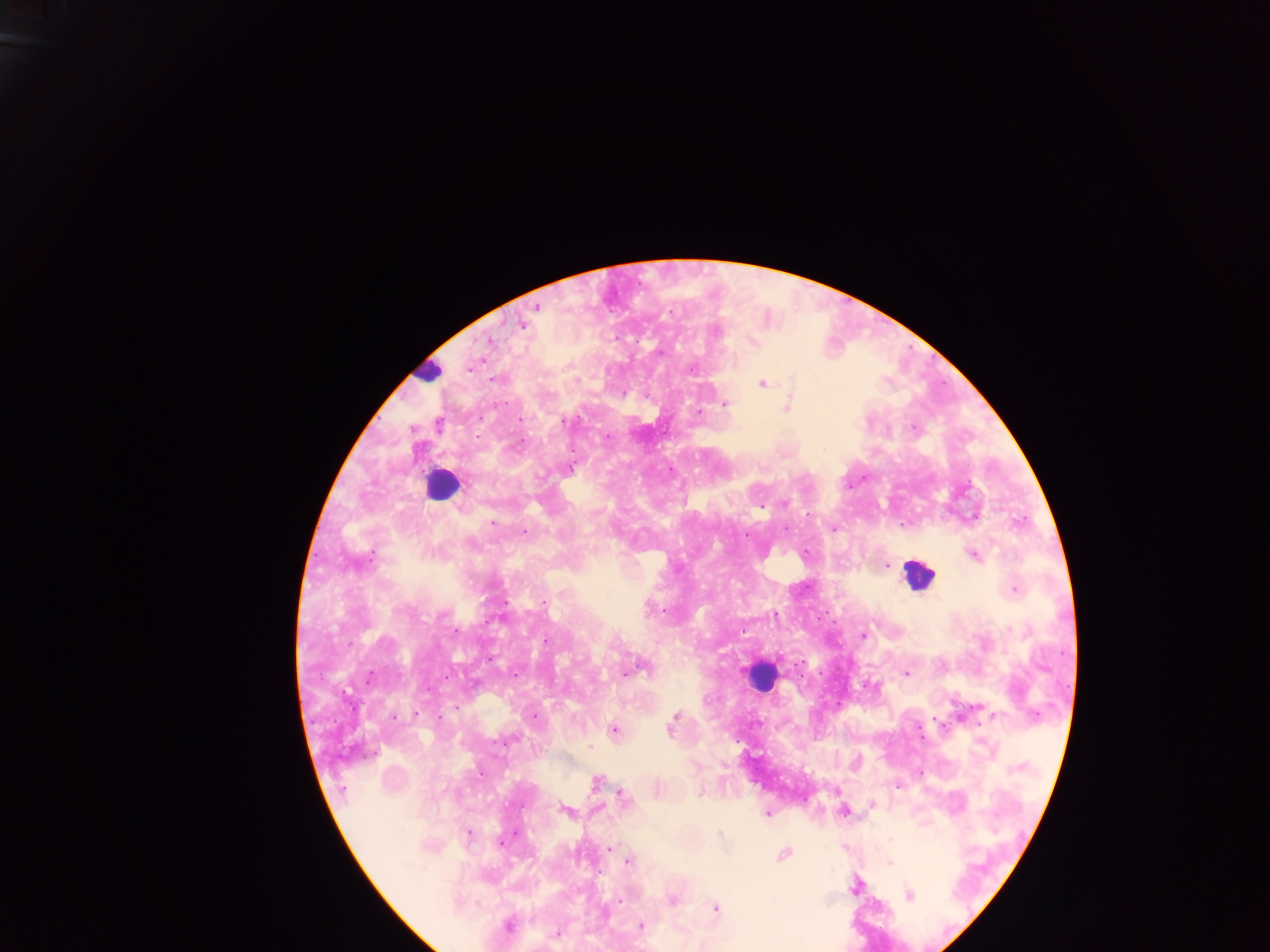 Approximate centers as (x, y) in pixels. Leukocyte locations: (427, 371), (442, 484), (918, 574), (761, 676). Malaria parasite locations: (536, 306), (521, 323), (717, 332), (490, 341), (754, 343), (493, 380), (763, 384), (724, 404), (786, 407), (519, 419), (563, 422), (439, 425), (607, 436), (571, 467), (784, 503), (493, 522), (833, 528), (524, 532), (973, 555), (372, 556), (887, 566), (1015, 589), (398, 611), (862, 635), (545, 642), (643, 668), (631, 671), (906, 674), (370, 675), (515, 675), (416, 714), (535, 716), (676, 716), (395, 717), (992, 717), (441, 718), (673, 722), (614, 730), (511, 740), (596, 782), (700, 793), (622, 798), (872, 804), (565, 810), (843, 811), (767, 813), (720, 834), (468, 835), (502, 841), (611, 849), (783, 855), (628, 861), (889, 863), (854, 887), (908, 895), (672, 899), (619, 900), (716, 908), (508, 925), (641, 926), (556, 935). Single field of view. Image is 1270×952 pixels. Thick blood film. Mobile-phone photograph taken through the microscope. Collected in Ghana.